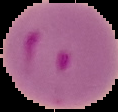

Image is 118×112 pixels. Segmented cell region on a black background. From a thin blood smear. Malaria status: parasitized.